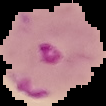

Summary:
  - Image size: 106×106 pixels
  - Result: Plasmodium parasites identified
  - Preparation: thin blood film
  - Image type: cell region segmented out of the field of view; surrounding area masked to black